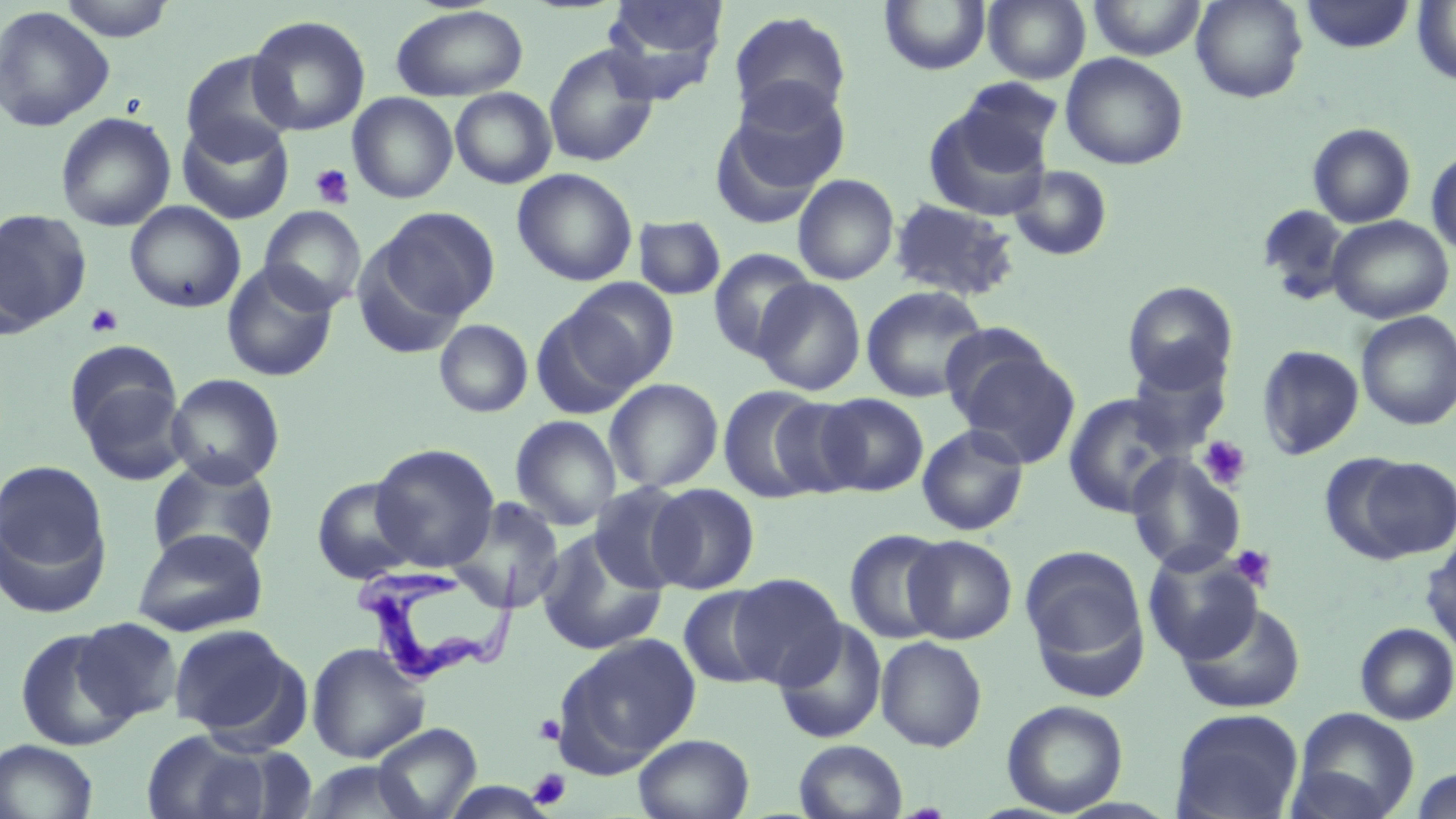
Summary:
  - Coordinate format: approximate bounding boxes as named x1/y1/x2/y2 corners in pixels
  - Uninfected red blood cell locations: (x1=57, y1=0, x2=177, y2=42), (x1=601, y1=0, x2=727, y2=99), (x1=880, y1=0, x2=990, y2=75), (x1=984, y1=0, x2=1091, y2=84), (x1=1087, y1=0, x2=1207, y2=60), (x1=1191, y1=0, x2=1308, y2=103), (x1=1299, y1=0, x2=1416, y2=54), (x1=1412, y1=1, x2=1456, y2=86), (x1=390, y1=4, x2=528, y2=101), (x1=0, y1=6, x2=115, y2=132), (x1=728, y1=10, x2=852, y2=126), (x1=247, y1=15, x2=371, y2=137), (x1=543, y1=44, x2=660, y2=167), (x1=180, y1=50, x2=298, y2=161), (x1=1060, y1=52, x2=1189, y2=170), (x1=955, y1=78, x2=1063, y2=171), (x1=725, y1=80, x2=852, y2=198), (x1=449, y1=88, x2=557, y2=189), (x1=348, y1=92, x2=458, y2=204), (x1=922, y1=102, x2=1055, y2=221), (x1=56, y1=112, x2=176, y2=232), (x1=176, y1=117, x2=294, y2=224), (x1=1307, y1=123, x2=1416, y2=228), (x1=1427, y1=147, x2=1456, y2=255), (x1=1009, y1=164, x2=1114, y2=262), (x1=512, y1=169, x2=638, y2=286), (x1=793, y1=174, x2=899, y2=285), (x1=888, y1=198, x2=1020, y2=301), (x1=125, y1=201, x2=246, y2=313), (x1=1256, y1=204, x2=1351, y2=303), (x1=259, y1=206, x2=365, y2=312), (x1=375, y1=206, x2=500, y2=324), (x1=0, y1=209, x2=92, y2=333), (x1=1326, y1=215, x2=1454, y2=324), (x1=633, y1=216, x2=726, y2=300), (x1=708, y1=248, x2=816, y2=359), (x1=221, y1=262, x2=338, y2=382), (x1=564, y1=278, x2=679, y2=391), (x1=752, y1=278, x2=865, y2=396), (x1=1122, y1=280, x2=1238, y2=393), (x1=861, y1=285, x2=989, y2=403), (x1=530, y1=304, x2=646, y2=420), (x1=1355, y1=311, x2=1456, y2=431), (x1=434, y1=319, x2=533, y2=418), (x1=64, y1=340, x2=181, y2=442), (x1=950, y1=341, x2=1082, y2=468), (x1=1256, y1=344, x2=1365, y2=460), (x1=1126, y1=355, x2=1232, y2=457), (x1=166, y1=373, x2=285, y2=487), (x1=604, y1=378, x2=723, y2=493), (x1=79, y1=381, x2=189, y2=486), (x1=718, y1=385, x2=828, y2=504), (x1=818, y1=393, x2=928, y2=495), (x1=1063, y1=393, x2=1185, y2=518), (x1=769, y1=399, x2=867, y2=500), (x1=510, y1=415, x2=622, y2=530), (x1=917, y1=424, x2=1029, y2=536), (x1=369, y1=443, x2=500, y2=571), (x1=1125, y1=453, x2=1246, y2=575), (x1=1344, y1=454, x2=1456, y2=562), (x1=147, y1=457, x2=279, y2=568), (x1=1, y1=460, x2=110, y2=595), (x1=311, y1=477, x2=421, y2=584), (x1=589, y1=481, x2=695, y2=593), (x1=647, y1=483, x2=760, y2=593), (x1=449, y1=497, x2=567, y2=614), (x1=131, y1=529, x2=269, y2=636), (x1=844, y1=529, x2=951, y2=644), (x1=535, y1=531, x2=668, y2=656), (x1=904, y1=535, x2=1018, y2=644), (x1=1421, y1=538, x2=1456, y2=658), (x1=1020, y1=546, x2=1149, y2=689), (x1=1143, y1=547, x2=1264, y2=665), (x1=728, y1=573, x2=845, y2=688), (x1=678, y1=585, x2=780, y2=689), (x1=1179, y1=602, x2=1307, y2=713), (x1=74, y1=617, x2=184, y2=724), (x1=774, y1=620, x2=887, y2=744), (x1=1355, y1=622, x2=1456, y2=725), (x1=169, y1=624, x2=300, y2=739), (x1=14, y1=627, x2=137, y2=750), (x1=554, y1=634, x2=701, y2=772), (x1=875, y1=636, x2=987, y2=752), (x1=306, y1=642, x2=429, y2=763), (x1=1001, y1=700, x2=1128, y2=816), (x1=1170, y1=708, x2=1304, y2=819), (x1=1288, y1=708, x2=1420, y2=819), (x1=371, y1=723, x2=481, y2=818), (x1=141, y1=729, x2=274, y2=819), (x1=633, y1=732, x2=755, y2=819), (x1=0, y1=739, x2=99, y2=819), (x1=794, y1=739, x2=908, y2=818), (x1=300, y1=761, x2=426, y2=819), (x1=1409, y1=767, x2=1456, y2=819)
  - Platelet locations: (x1=309, y1=164, x2=355, y2=208), (x1=84, y1=303, x2=124, y2=338), (x1=1197, y1=436, x2=1251, y2=490), (x1=1229, y1=544, x2=1277, y2=591), (x1=534, y1=714, x2=565, y2=746), (x1=528, y1=768, x2=570, y2=809)
  - Trypanosoma brucei locations: (x1=356, y1=563, x2=513, y2=689)
  - Slide-level diagnosis: Trypanosoma brucei
  - Image size: 1456×819 pixels
  - Preparation: thin blood smear
  - Modality: optical microscopy
  - Stain: May-Grünwald-Giemsa
  - Field of view: single
  - Magnification: 1000x